Locate every blood parasite and identify its species.
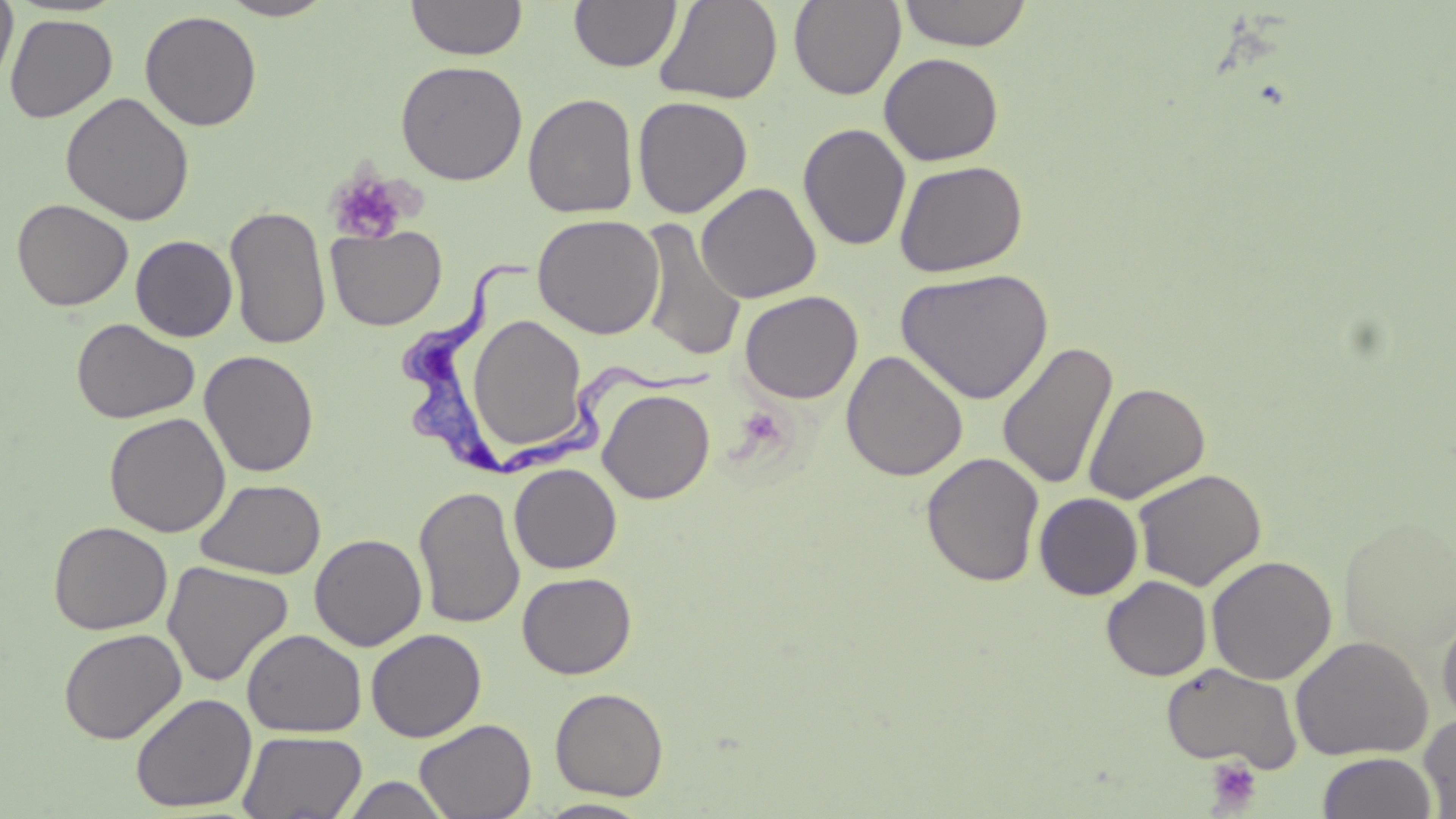
Approximate bounding boxes as [x1, y1, x2, y2] in pixels.
Trypanosoma brucei: [398, 243, 505, 476], [506, 365, 714, 477].
No Plasmodium falciparum, Plasmodium ovale, Plasmodium malariae, Plasmodium vivax, or Babesia divergens observed.

{
  "slide_level_diagnosis": "Trypanosoma brucei",
  "stain": "May-Grünwald-Giemsa",
  "preparation": "thin blood film",
  "magnification": "1000x",
  "platelet_locations": "approximate bounding boxes as [x1, y1, x2, y2] in pixels: [326, 169, 409, 246], [1205, 756, 1262, 812]",
  "field_of_view": "single",
  "uninfected_red_blood_cell_locations": "approximate bounding boxes as [x1, y1, x2, y2] in pixels: [0, 0, 17, 91], [217, 0, 336, 20], [406, 0, 528, 60], [569, 0, 681, 73], [654, 0, 783, 105], [898, 0, 1033, 50], [789, 1, 905, 100], [140, 10, 262, 131], [4, 13, 117, 123], [879, 52, 1004, 166], [395, 60, 528, 185], [60, 92, 195, 226], [523, 93, 638, 218], [632, 96, 752, 218], [798, 123, 911, 251], [894, 159, 1027, 277], [695, 182, 822, 303], [11, 198, 133, 311], [224, 205, 332, 350], [532, 214, 665, 339], [638, 217, 747, 363], [326, 225, 447, 330], [130, 235, 237, 342], [896, 268, 1054, 404], [739, 290, 863, 404], [465, 311, 591, 459], [71, 318, 199, 424], [997, 339, 1118, 491], [841, 349, 968, 481], [199, 350, 319, 477], [1083, 381, 1210, 504], [598, 388, 715, 505], [104, 412, 230, 537], [921, 451, 1045, 588], [509, 462, 622, 574], [1132, 468, 1268, 591], [195, 478, 326, 579], [413, 485, 525, 630], [1034, 492, 1143, 600], [1338, 514, 1456, 664], [48, 521, 172, 635], [310, 533, 427, 651], [1206, 554, 1337, 685], [162, 561, 293, 688], [517, 571, 636, 679], [1101, 575, 1212, 681], [1436, 610, 1456, 728], [58, 628, 186, 744], [241, 628, 367, 738], [366, 628, 486, 742], [1290, 635, 1432, 761], [1160, 662, 1303, 772], [550, 687, 669, 801], [130, 692, 257, 812], [1419, 713, 1456, 817], [414, 718, 536, 819], [237, 730, 367, 818], [1317, 752, 1438, 819], [338, 776, 452, 818], [534, 798, 655, 818]",
  "image_size": "1456×819 pixels",
  "modality": "light microscopy"
}